Assess this cell for malaria.
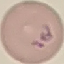

Parasitized.

{
  "preparation": "thin smear",
  "stain": "Giemsa",
  "image_type": "cell patch, automatically extracted from a larger field of view and resized to 64 × 64 pixels",
  "capture": "smartphone through the microscope eyepiece"
}